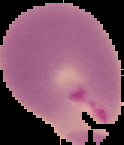

{
  "preparation": "thin blood smear",
  "image_type": "cell region segmented out of the field of view; surrounding area masked to black",
  "image_size": "124×145 pixels",
  "result": "Plasmodium parasites identified"
}